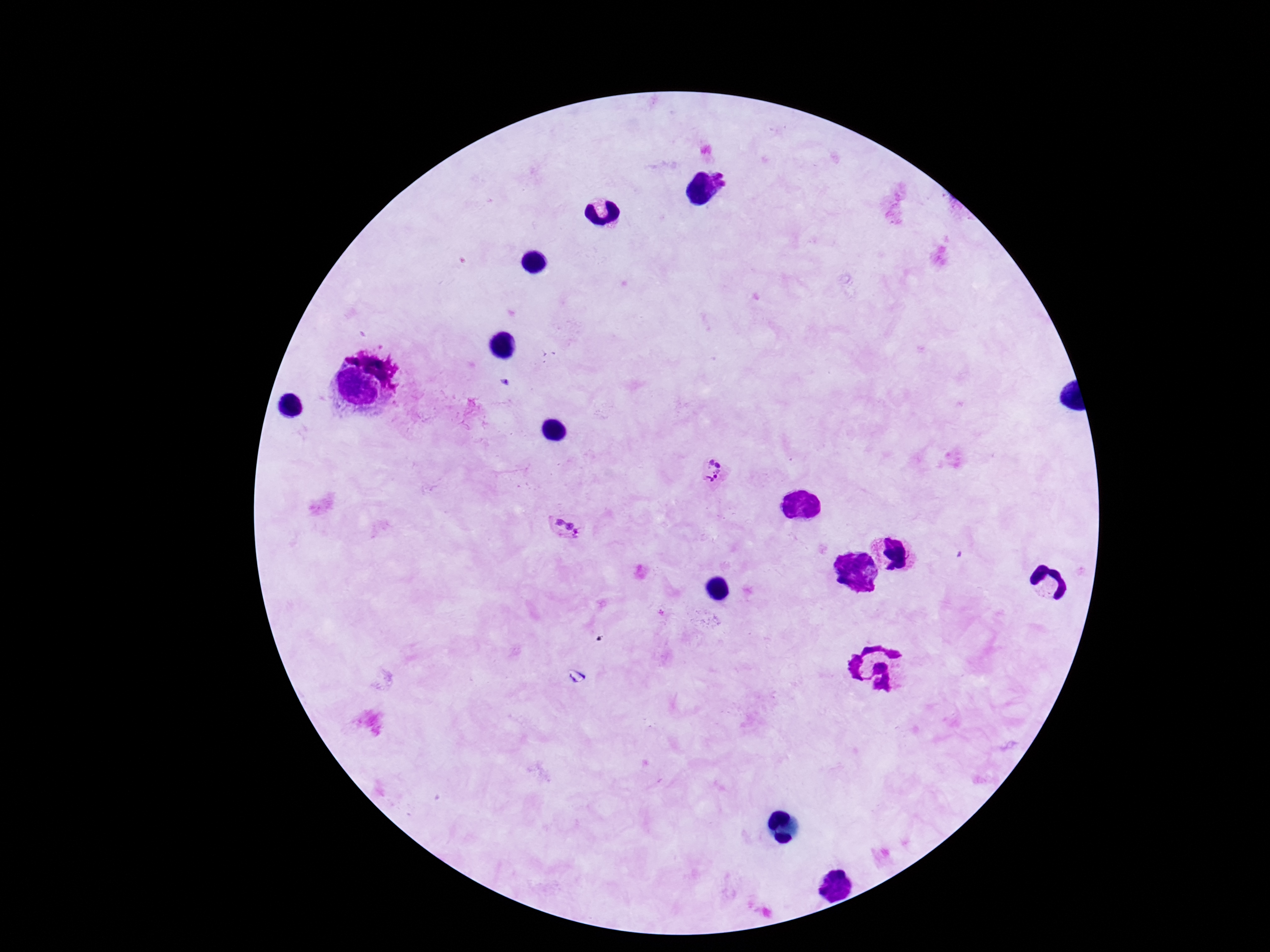
Approximate centers as {x, y} in pixels. Plasmodium parasite locations: {724, 176}, {716, 473}, {565, 528}. Image is 1270×952 pixels. Patient malaria status: positive. 100x magnification. One field from this slide. Thick blood film. Giemsa-stained preparation. Photographed through the microscope eyepiece with a smartphone camera.